State which parasite is depicted.
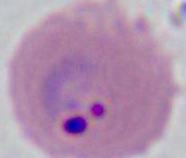
This is Plasmodium.

400x or 1000x magnification. Micrograph.